Report the malaria status of this cell.
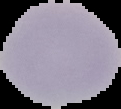
It is uninfected.

From a thin blood film. Segmented cell region on a black background. Image is 121×109 pixels.